Report the malaria status of this cell.
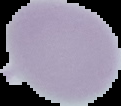

It is uninfected.

{
  "image_type": "segmented cell region on a black background",
  "preparation": "thin blood smear",
  "image_size": "121×106 pixels"
}